Report the malaria status of this cell.
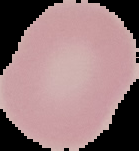

Uninfected.

Cell region segmented out of the field of view; the surrounding area is masked to black. Image is 139×151 pixels. From a thin blood smear.